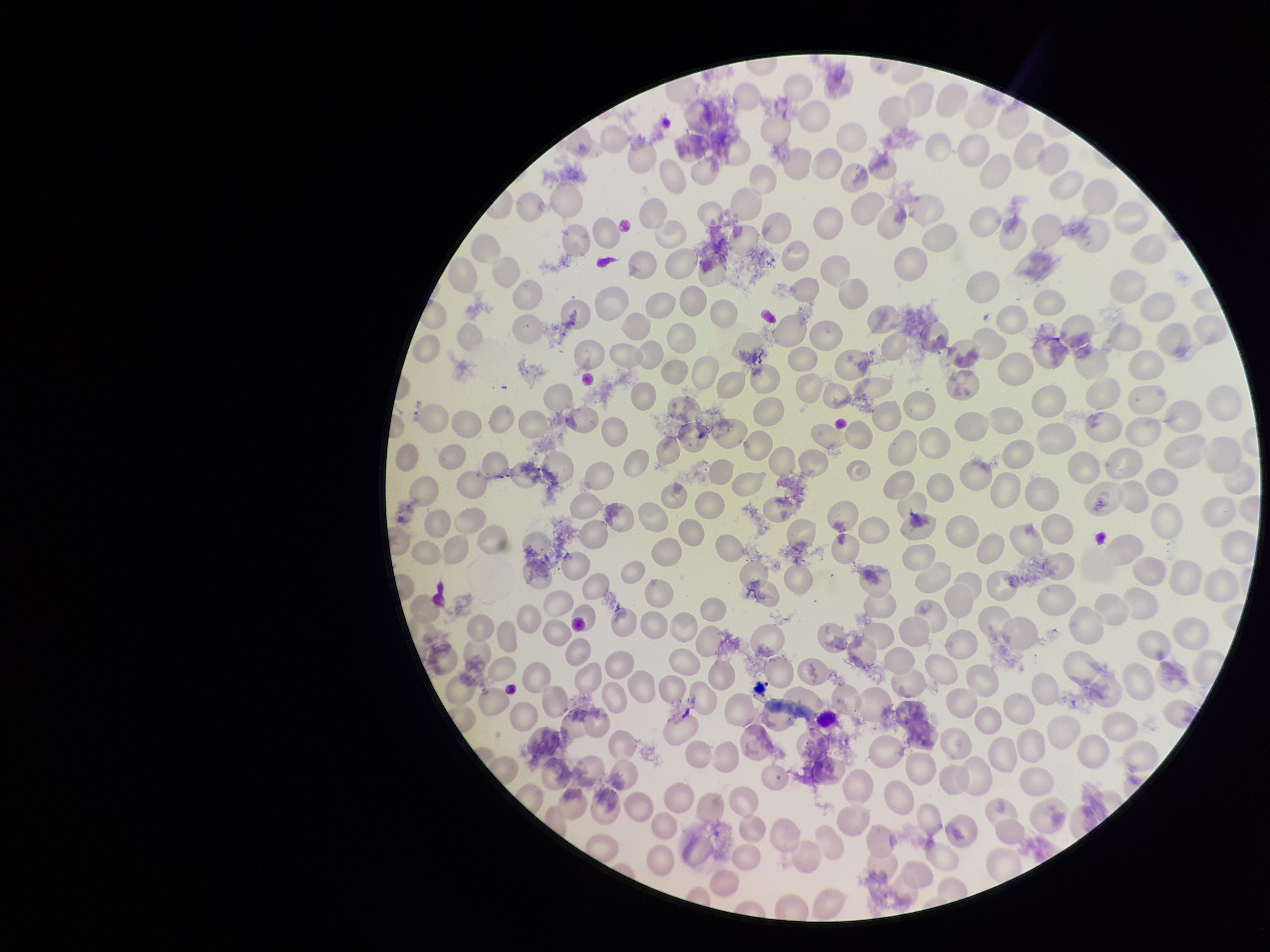

Summary:
  - Species reported for this patient: Plasmodium falciparum
  - Parasitized red blood cells: none detected
  - Red blood cell count: 191
  - Capture: smartphone photograph through the microscope eyepiece
  - Parasitized red blood cell count: 0
  - Image size: 1270×952 pixels
  - Preparation: thin blood smear
  - Stain: Giemsa
  - Field of view: single
  - Patient malaria status: infected